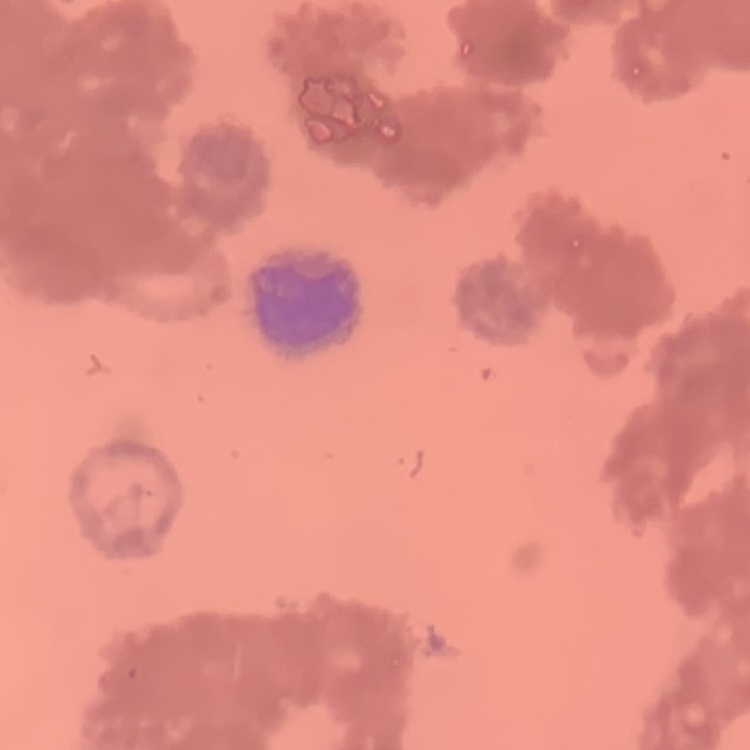

The erythrocytes show rouleaux formation. Field's or Giemsa stain. Thin blood smear. One tile cut from a larger photomicrograph.